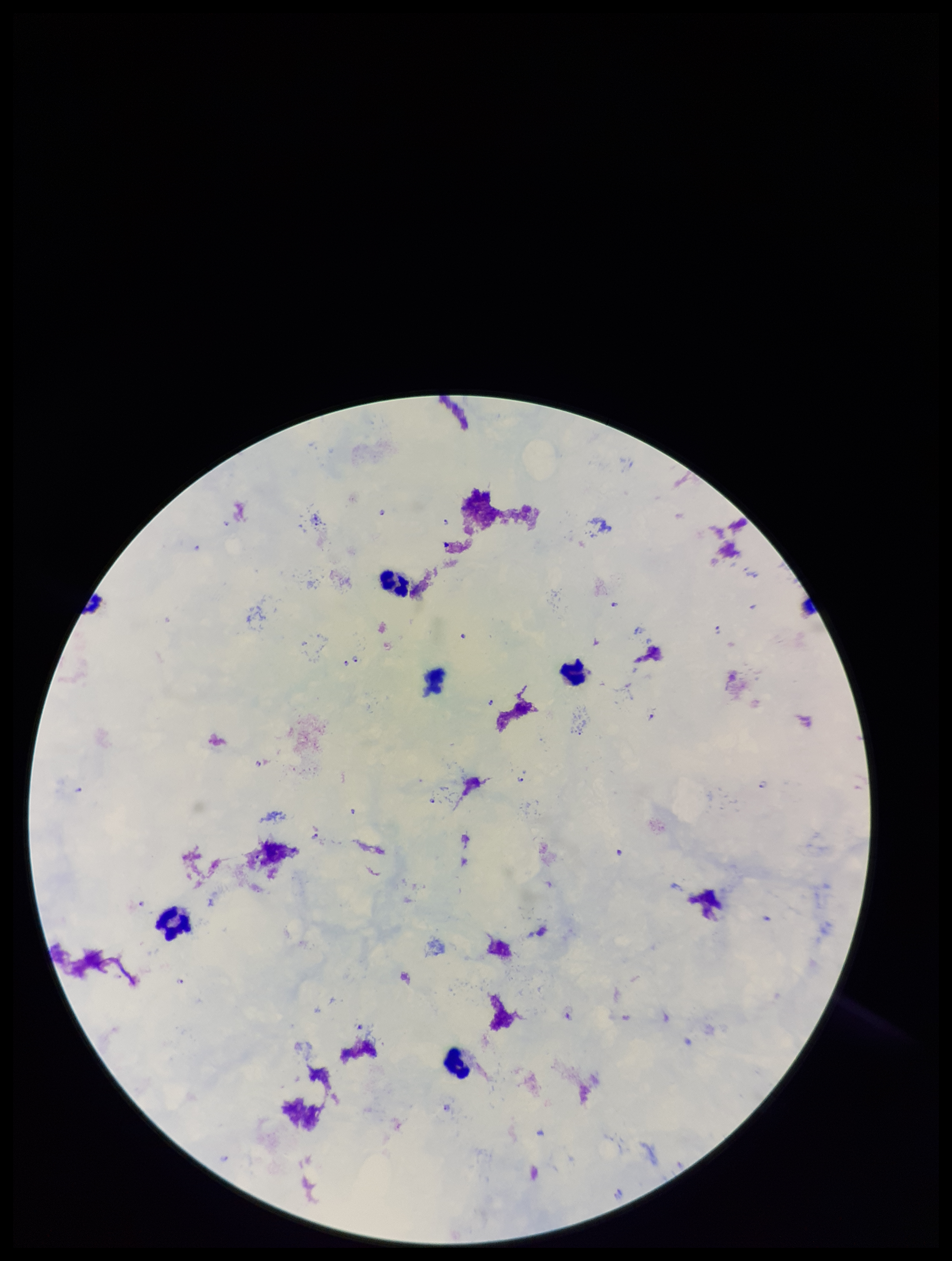 Stained with Giemsa. Plasmodium parasites: seen. One field from this slide. Patient malaria status: positive. Smartphone photograph taken through the eyepiece of a microscope. Parasite count: 14. Image is 952×1261 pixels. Leukocyte count: 4. Species reported for this patient: Plasmodium falciparum. Preparation: thick smear.